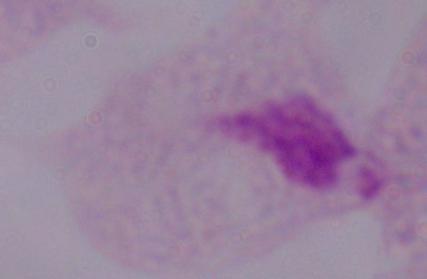
Micrograph. 1000x magnification. A trichomonad is shown.